Locate every blood parasite and identify its species.
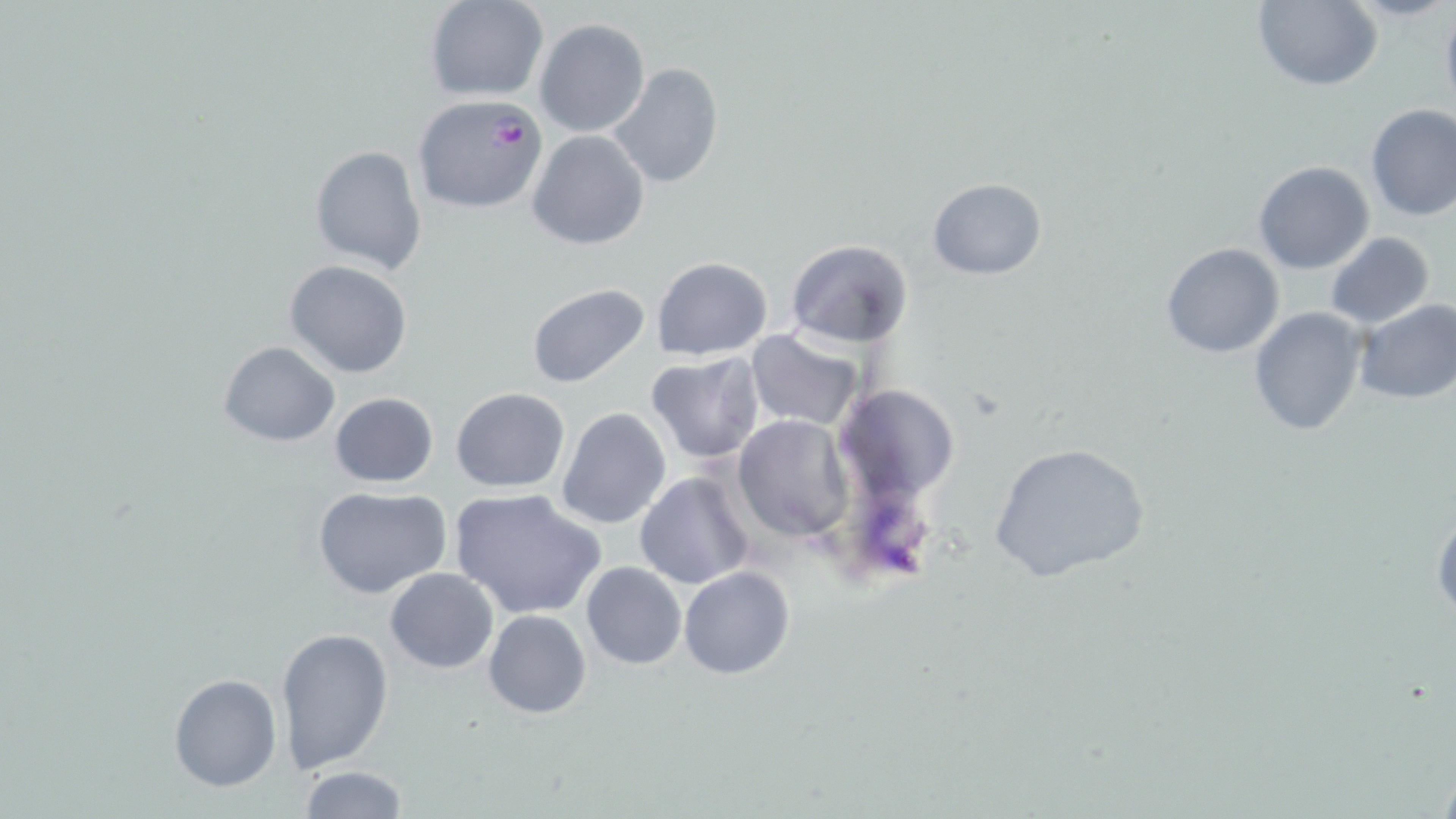
Approximate bounding boxes as (x1,y1)-(x2,y2) corner pairs in pixels.
Plasmodium falciparum-infected red blood cells: (409,93)-(550,214).
No Plasmodium ovale, Plasmodium malariae, Plasmodium vivax, Babesia divergens, or Trypanosoma brucei observed.

slide-level diagnosis = Plasmodium falciparum
modality = light microscopy
field of view = one of a larger specimen
uninfected red blood cell locations = approximate bounding boxes as (x1,y1)-(x2,y2) corner pairs in pixels: (1249,0)-(1383,91), (425,1)-(547,101), (1439,5)-(1456,119), (534,17)-(650,137), (609,62)-(723,189), (1364,103)-(1455,222), (526,129)-(651,250), (309,143)-(427,276), (1253,161)-(1374,275), (927,176)-(1047,280), (1323,232)-(1435,329), (785,239)-(913,348), (1159,242)-(1286,359), (652,256)-(773,361), (285,259)-(414,379), (525,283)-(652,389), (1353,300)-(1456,405), (1248,305)-(1368,437), (746,329)-(866,432), (216,341)-(340,447), (644,352)-(766,466), (835,383)-(962,507), (451,388)-(569,493), (328,392)-(439,488), (557,407)-(672,530), (733,415)-(854,541), (987,441)-(1153,587), (633,472)-(759,591), (313,486)-(454,601), (449,488)-(605,619), (1430,500)-(1455,621), (581,562)-(686,670), (678,566)-(796,680), (384,567)-(499,674), (483,609)-(592,719), (277,627)-(394,772), (168,674)-(282,791), (293,766)-(412,819)
magnification = 1000x
preparation = thin blood smear
image size = 1456×819 pixels
stain = May-Grünwald-Giemsa